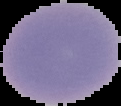
preparation = thin blood smear
image size = 121×106 pixels
image type = cell region segmented out of the field of view; surrounding area masked to black
malaria status = uninfected